Assess this cell for malaria.
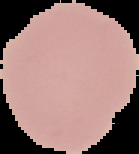

Uninfected.

From a thin blood smear. Image is 139×154 pixels. Cell region segmented out of the field of view; the surrounding area is masked to black.